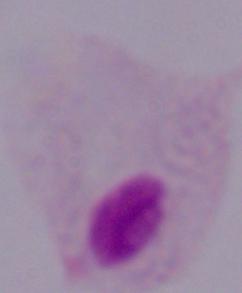 Photomicrograph. 1000x magnification. A trichomonad is shown.